Assess the morphology of the erythrocytes.
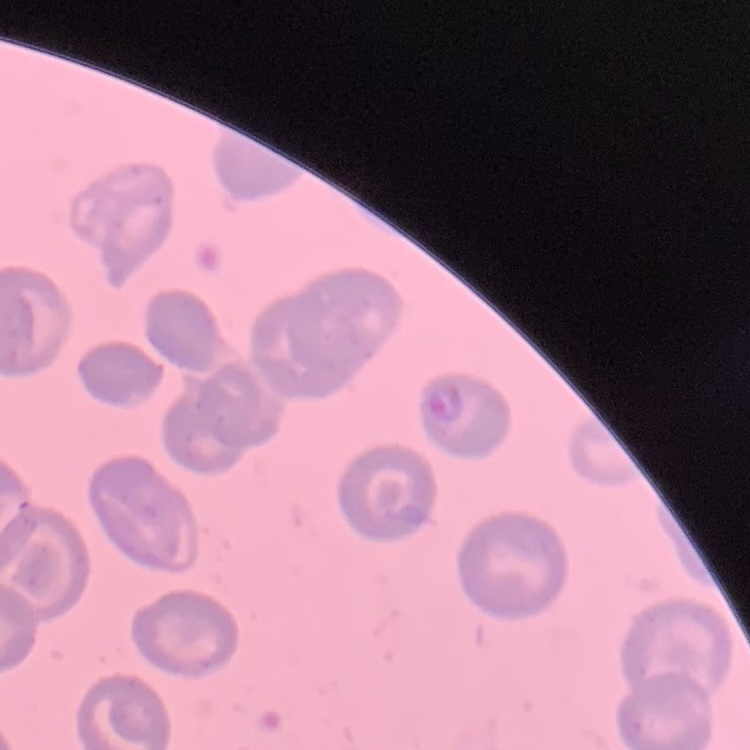

They show no rouleaux formation.

Stained with either Field's or Giemsa. One tile cut from a larger photomicrograph. Thin blood film.